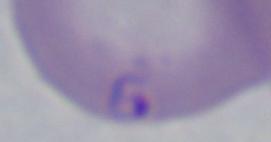
Summary:
  - Modality: micrograph
  - Magnification: 1000x
  - Identification: Babesia